Report the malaria status of this cell.
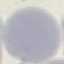
It is uninfected.

Giemsa-stained preparation. Acquired by smartphone through the microscope eyepiece. Automatically extracted cell patch, resized to 64 × 64 pixels. Thin smear of blood.